State the blood parasite species.
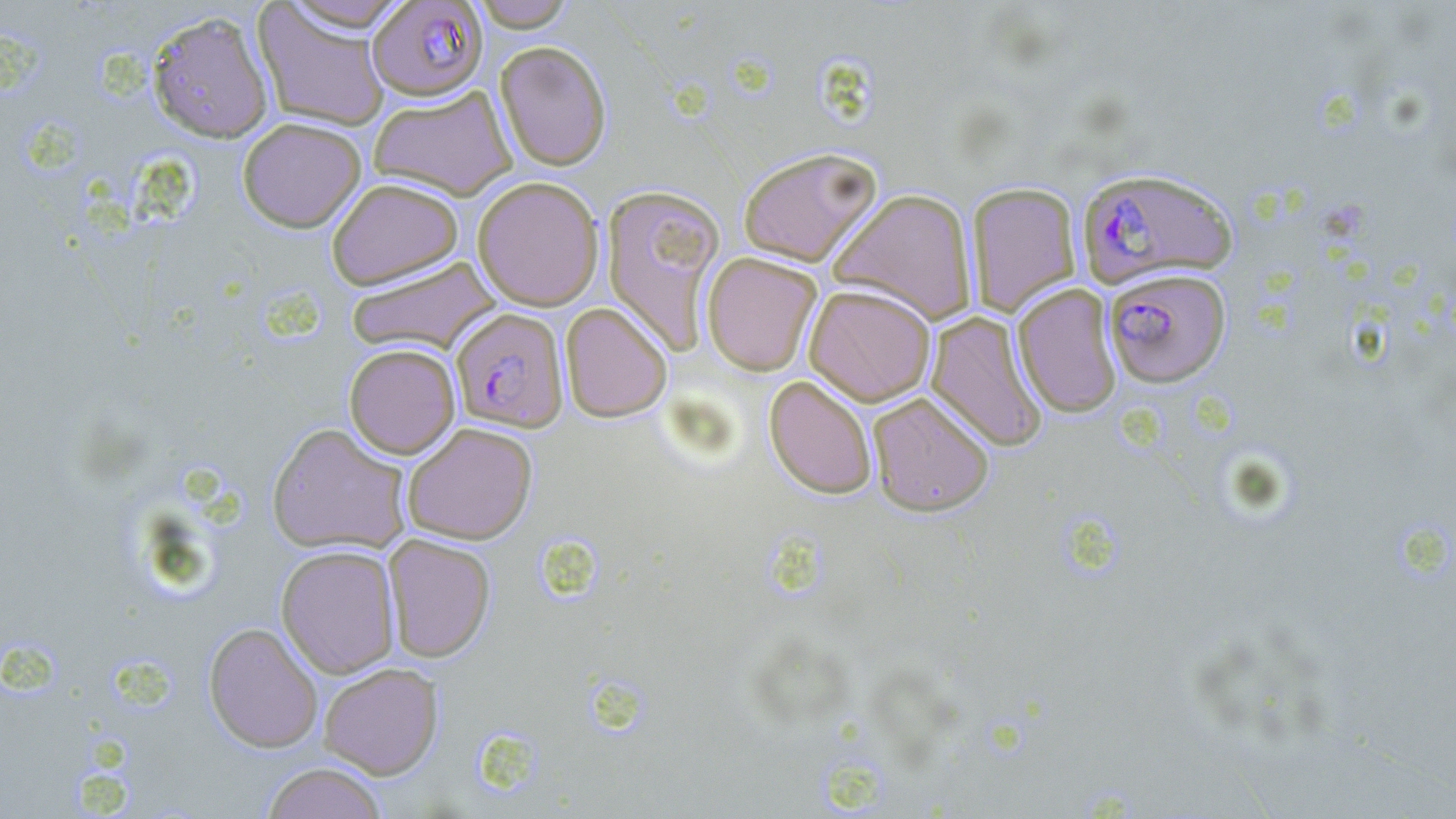

Plasmodium falciparum.

Approximate bounding boxes as (x1,y1)-(x2,y2) corner pairs in pixels. Plasmodium falciparum-infected red blood cell locations: (367,0)-(489,101), (1076,166)-(1237,289), (1104,268)-(1231,387), (451,307)-(568,432). Uninfected red blood cell locations: (278,0)-(414,32), (469,0)-(576,31), (253,3)-(391,131), (147,9)-(275,144), (494,41)-(612,170), (368,86)-(518,200), (238,117)-(367,232), (738,147)-(881,266), (472,176)-(604,311), (326,177)-(464,289), (966,182)-(1081,317), (601,183)-(726,354), (828,188)-(977,325), (702,251)-(822,376), (345,256)-(500,355), (804,283)-(936,406), (1012,284)-(1122,418), (560,301)-(672,422), (926,311)-(1048,451), (344,343)-(461,459), (764,375)-(878,499), (868,392)-(995,516), (267,422)-(412,555), (402,423)-(538,544), (383,534)-(496,662), (276,544)-(400,678), (203,622)-(324,752), (319,662)-(444,779), (261,762)-(388,819). One field of a larger specimen. May-Grünwald-Giemsa-stained preparation. 1000x magnification. Image is 1456×819 pixels. Thin blood film. Light microscopy.